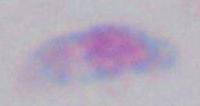

Photomicrograph. Toxoplasma gondii is shown. 1000x magnification.